Identify the blood parasite species.
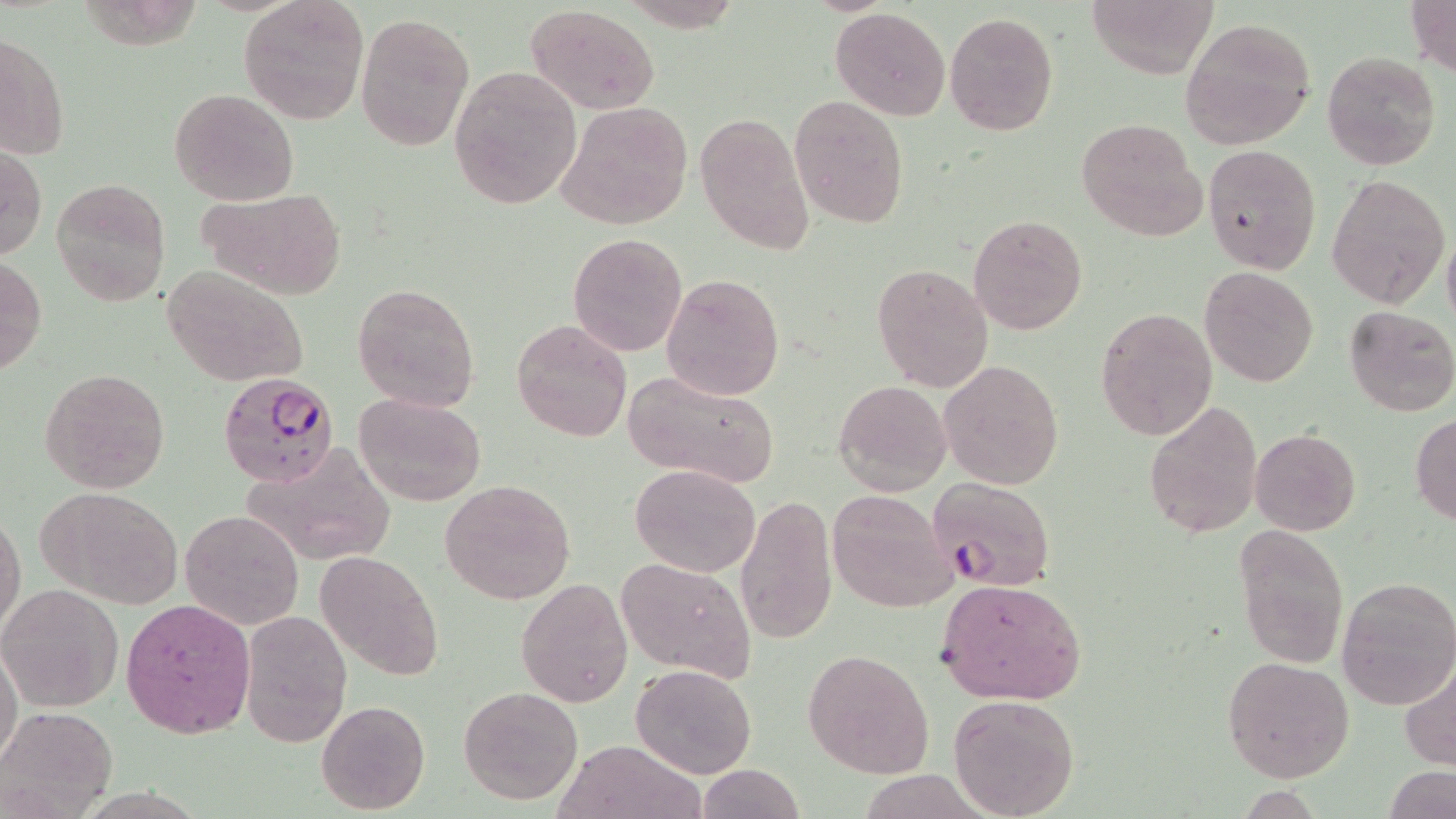
Plasmodium falciparum.

Approximate bounding boxes as (x1,y1)-(x2,y2) corner pairs in pixels. Plasmodium falciparum-infected red blood cell locations: (217,373)-(343,488), (928,477)-(1054,591). Uninfected red blood cell locations: (238,0)-(367,124), (1087,0)-(1216,78), (1408,0)-(1456,79), (524,4)-(660,114), (832,7)-(950,121), (944,11)-(1061,136), (355,12)-(474,151), (1179,18)-(1316,150), (2,28)-(70,163), (1322,50)-(1441,172), (449,66)-(582,210), (168,89)-(298,205), (789,95)-(908,227), (557,101)-(693,229), (695,109)-(816,255), (1076,116)-(1207,240), (1203,143)-(1322,275), (1,145)-(46,260), (1327,174)-(1450,308), (50,178)-(172,306), (196,186)-(349,299), (969,214)-(1087,333), (1442,229)-(1456,335), (568,234)-(687,357), (0,254)-(46,377), (872,262)-(994,393), (163,265)-(309,387), (1200,266)-(1320,387), (661,273)-(784,401), (353,282)-(480,413), (1343,304)-(1456,417), (1096,306)-(1218,443), (511,320)-(631,441), (938,360)-(1063,488), (39,368)-(171,493), (622,369)-(780,489), (833,381)-(952,497), (354,392)-(486,506), (1143,401)-(1263,542), (1410,413)-(1456,524), (1249,428)-(1361,535), (243,443)-(396,565), (631,463)-(760,577), (667,468)-(805,612), (440,479)-(575,605), (33,486)-(186,608), (825,489)-(957,609), (736,491)-(838,645), (0,509)-(26,638), (181,510)-(303,628), (1232,524)-(1350,670), (314,549)-(442,680), (615,557)-(756,681), (516,578)-(633,706), (935,578)-(1085,704), (1336,578)-(1456,708), (1,583)-(124,713), (121,599)-(256,739), (239,611)-(353,748), (0,643)-(22,774), (801,649)-(935,777), (1223,655)-(1353,782), (1401,659)-(1456,771), (632,664)-(757,778), (457,685)-(583,805), (946,693)-(1080,819), (316,699)-(430,813), (1,706)-(116,817), (555,739)-(706,819), (696,764)-(804,819). Single field of view. Captured at 1000x magnification. Image is 1456×819 pixels. Light microscopy. May-Grünwald-Giemsa stain. Thin blood film.